Assess the morphology of the erythrocytes.
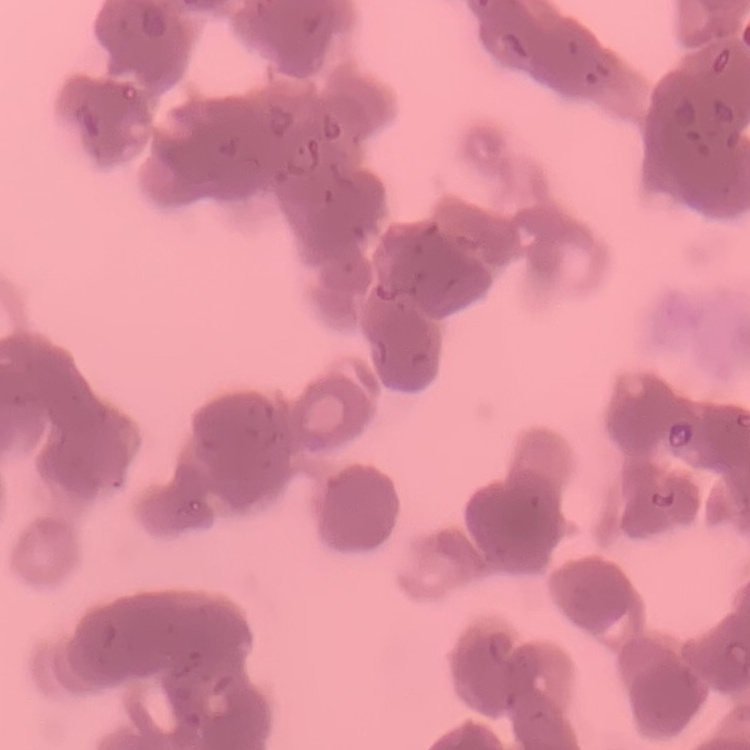
They show rouleaux formation.

stain: Field's or Giemsa
preparation: thin blood film
image_type: square crop of a larger photomicrograph